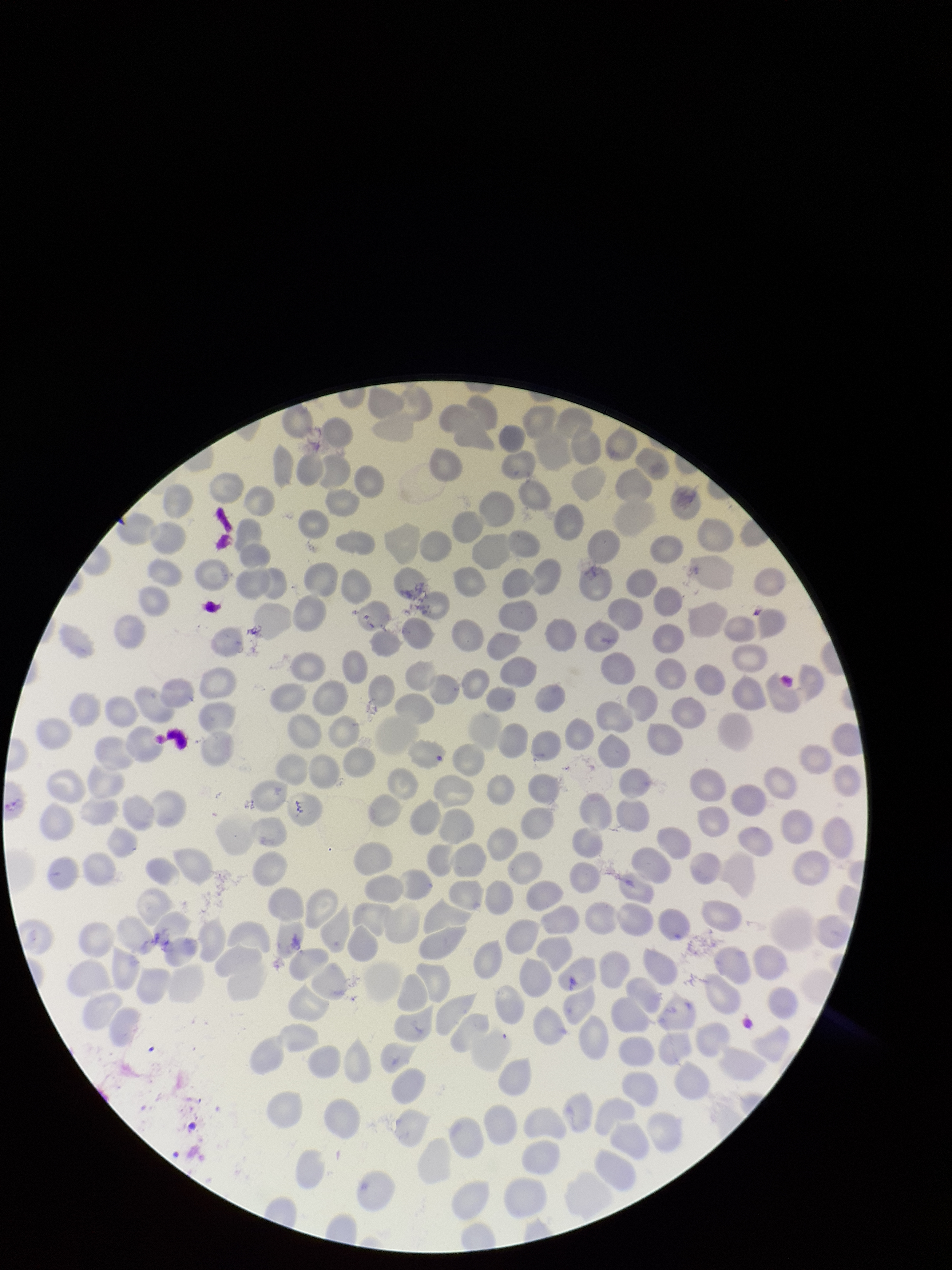
Summary:
  - Patient malaria status: infected
  - Parasitized red blood cells: none identified
  - Red blood cell count: 239
  - Species reported for this patient: Plasmodium falciparum
  - Image size: 952×1270 pixels
  - Capture: smartphone photograph through the microscope eyepiece
  - Stain: Giemsa
  - Preparation: thin
  - Field of view: single
  - Parasitized red blood cell count: 0